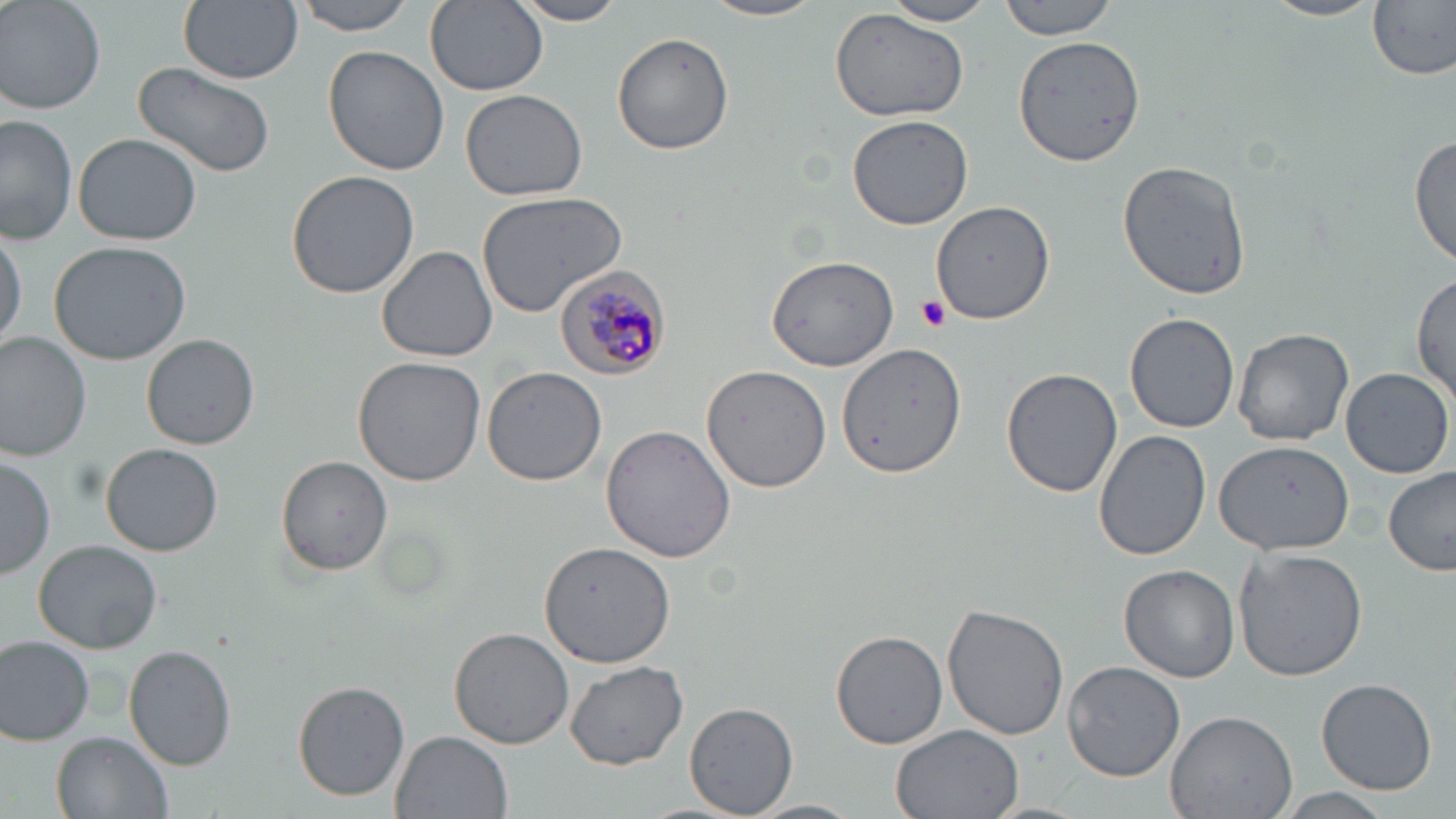
slide-level diagnosis = Plasmodium malariae
stain = May-Grünwald-Giemsa
field of view = one of a larger specimen
magnification = 1000x
uninfected red blood cell locations = approximate bounding boxes as [x1, y1, x2, y2] in pixels: [1, 0, 105, 114], [180, 0, 302, 85], [290, 0, 420, 34], [425, 0, 548, 96], [508, 0, 632, 25], [704, 0, 829, 22], [883, 0, 999, 26], [997, 0, 1121, 39], [1263, 0, 1381, 23], [1367, 1, 1455, 79], [830, 9, 973, 125], [611, 31, 735, 155], [1013, 32, 1145, 168], [325, 47, 451, 177], [135, 64, 276, 177], [459, 88, 587, 202], [1, 114, 78, 246], [846, 114, 973, 230], [73, 133, 203, 244], [1412, 133, 1455, 272], [1118, 160, 1252, 300], [287, 171, 419, 298], [477, 190, 631, 318], [931, 200, 1056, 323], [0, 219, 25, 352], [48, 239, 192, 365], [377, 245, 498, 362], [764, 252, 899, 372], [1412, 272, 1455, 412], [1126, 314, 1240, 434], [1233, 327, 1355, 444], [0, 332, 94, 460], [143, 334, 259, 450], [837, 343, 964, 478], [353, 356, 486, 487], [701, 365, 832, 493], [482, 366, 607, 486], [1341, 366, 1453, 478], [1001, 368, 1124, 498], [600, 424, 735, 562], [1094, 429, 1211, 560], [1216, 440, 1354, 554], [102, 443, 223, 557], [0, 453, 54, 580], [275, 456, 392, 575], [1382, 468, 1456, 577], [540, 538, 674, 667], [34, 540, 164, 654], [1234, 547, 1366, 681], [1119, 564, 1240, 681], [943, 603, 1071, 740], [449, 626, 574, 750], [829, 629, 947, 751], [0, 633, 98, 746], [125, 643, 237, 771], [564, 661, 689, 770], [1062, 661, 1185, 782], [1316, 679, 1437, 795], [294, 682, 408, 802], [684, 702, 799, 817], [1166, 708, 1298, 819], [890, 725, 1023, 819], [389, 730, 512, 818], [52, 732, 172, 819], [1268, 790, 1400, 819], [747, 799, 863, 819]
platelet locations = approximate bounding boxes as [x1, y1, x2, y2] in pixels: [915, 295, 951, 331]
preparation = thin blood film
Plasmodium malariae-infected red blood cell locations = approximate bounding boxes as [x1, y1, x2, y2] in pixels: [556, 267, 670, 379]
modality = optical microscopy
image size = 1456×819 pixels